Report the malaria status of this cell.
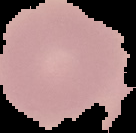
It is uninfected.

Summary:
  - Preparation: thin blood film
  - Image size: 136×133 pixels
  - Image type: cell region segmented out of the field of view; surrounding area masked to black